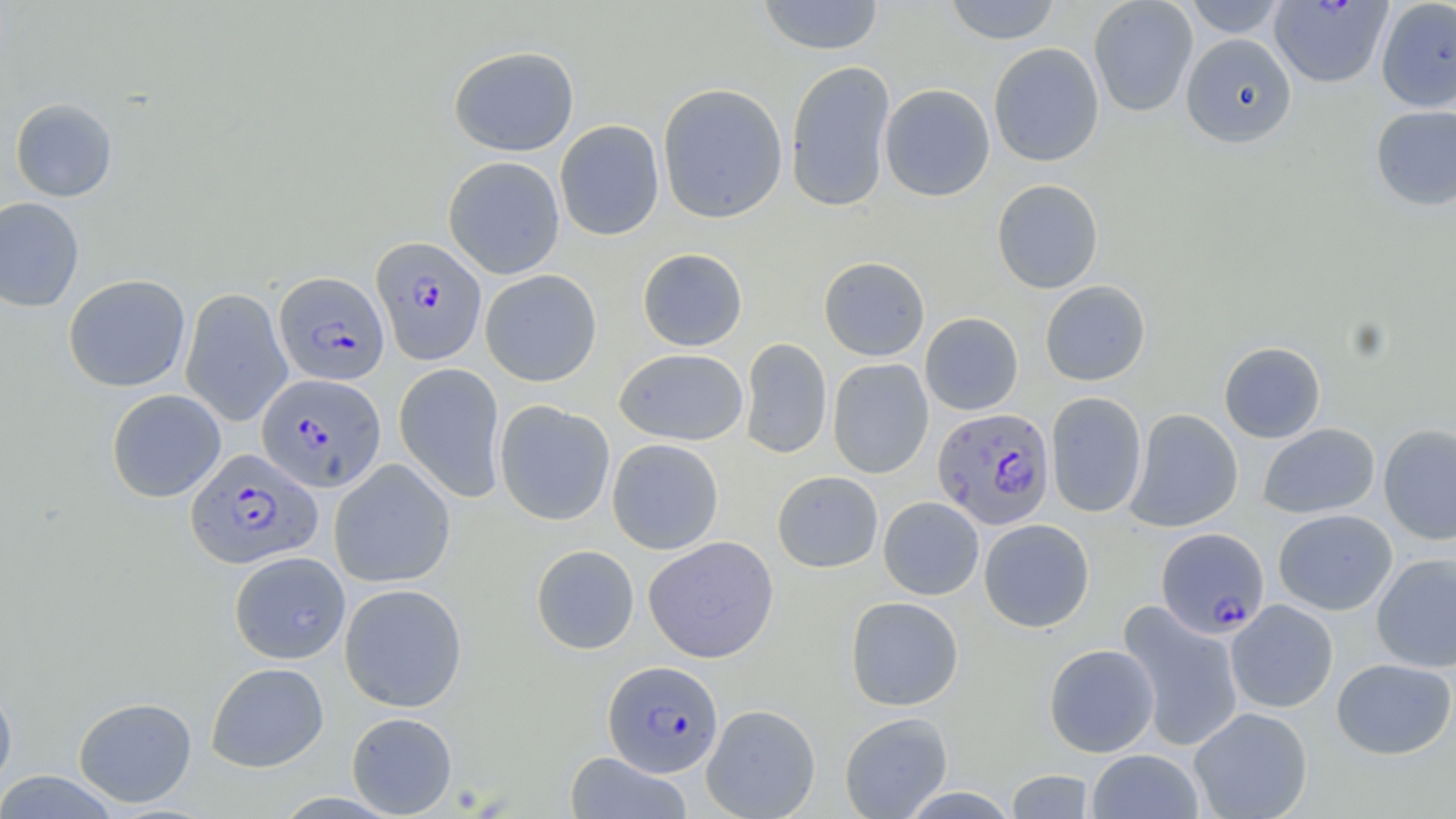
Approximate bounding boxes as [x1, y1, x2, y2] in pixels. Uninfected red blood cell locations: [757, 0, 884, 56], [944, 0, 1061, 44], [1089, 0, 1198, 117], [1182, 0, 1288, 37], [1375, 0, 1456, 112], [1180, 33, 1297, 148], [988, 42, 1104, 167], [448, 45, 580, 156], [785, 60, 896, 213], [657, 82, 788, 223], [880, 83, 995, 201], [10, 98, 117, 202], [1370, 105, 1456, 210], [554, 120, 665, 241], [443, 156, 565, 279], [991, 179, 1104, 294], [0, 196, 84, 312], [638, 248, 748, 351], [818, 256, 930, 361], [480, 269, 602, 386], [63, 274, 191, 392], [1040, 280, 1151, 386], [180, 288, 292, 427], [920, 312, 1023, 415], [739, 337, 832, 460], [1219, 341, 1326, 443], [614, 348, 749, 446], [828, 359, 933, 479], [394, 362, 506, 503], [107, 389, 226, 502], [1046, 392, 1148, 517], [494, 401, 615, 526], [1124, 408, 1243, 532], [1258, 423, 1380, 519], [1378, 423, 1456, 546], [607, 438, 724, 554], [329, 458, 455, 588], [772, 471, 883, 572], [878, 496, 984, 600], [1273, 509, 1397, 615], [978, 519, 1095, 632], [643, 536, 779, 663], [531, 545, 639, 654], [229, 551, 350, 664], [1371, 553, 1456, 673], [339, 583, 468, 712], [845, 596, 964, 711], [1226, 599, 1338, 713], [1118, 601, 1244, 752], [1044, 643, 1159, 757], [1331, 658, 1455, 759], [206, 662, 329, 772], [0, 681, 17, 793], [73, 696, 197, 807], [701, 703, 821, 819], [1189, 707, 1313, 819], [346, 711, 458, 817], [839, 711, 953, 818], [1086, 749, 1204, 818], [564, 752, 693, 818], [1006, 769, 1096, 818], [0, 771, 121, 818], [902, 787, 1016, 818]. Plasmodium falciparum-infected red blood cell locations: [1269, 0, 1394, 89], [371, 236, 487, 365], [275, 271, 389, 386], [256, 373, 386, 492], [932, 407, 1055, 530], [186, 448, 321, 570], [1156, 527, 1269, 638], [604, 660, 723, 777]. Slide-level diagnosis: Plasmodium falciparum. Thin blood smear. One field of a larger specimen. May-Grünwald-Giemsa stain. Captured at 1000x magnification. Optical microscopy. Image is 1456×819 pixels.